Give the extent of all Plasmodium ovale-infected red blood cells.
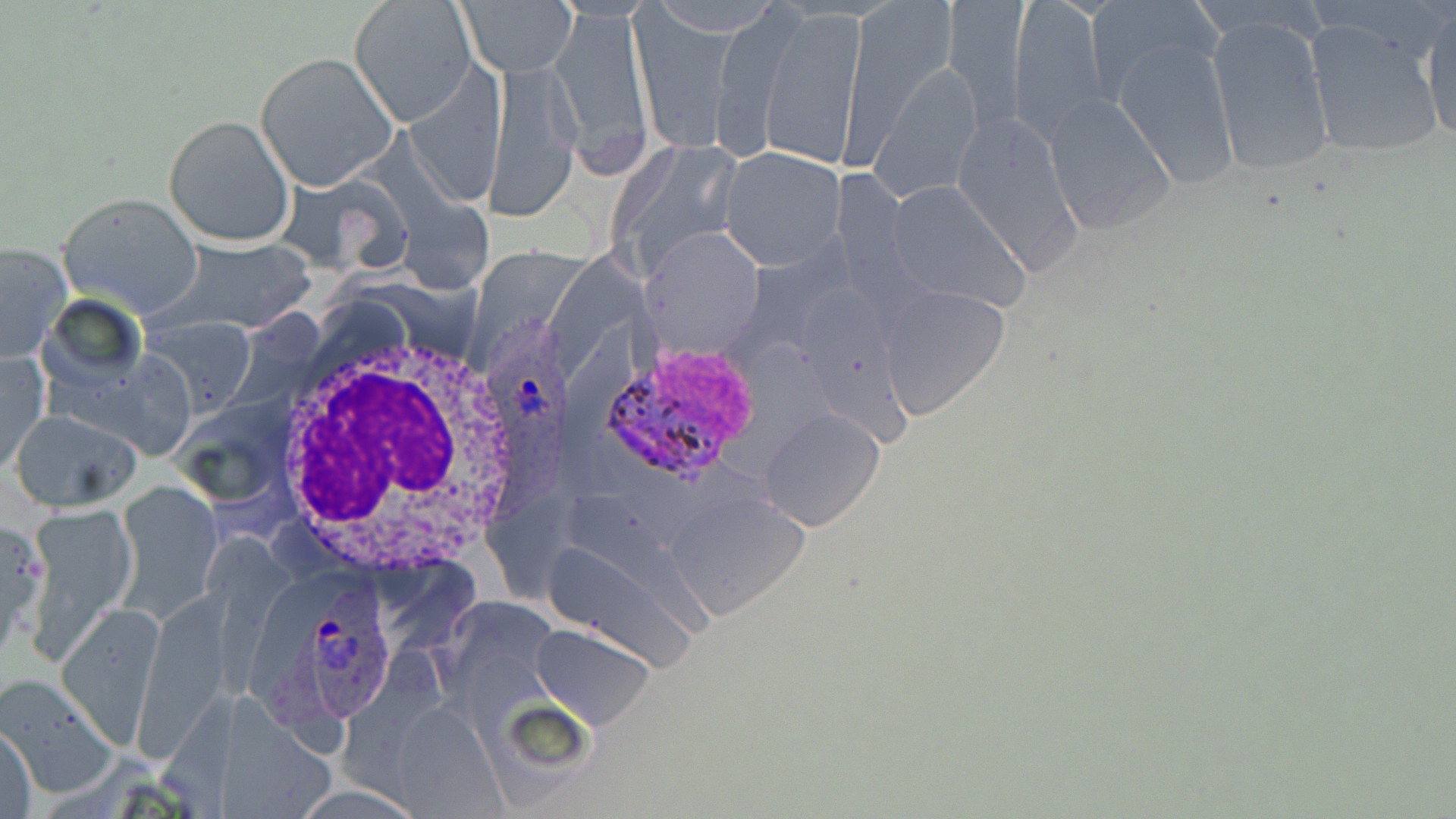
Approximate bounding boxes as (x1, y1, x2, y2) in pixels.
Plasmodium ovale-infected red blood cells: (484, 307, 573, 531), (592, 340, 761, 484), (253, 573, 399, 738).

Summary:
  - Uninfected red blood cell locations: (844, 0, 962, 152), (1008, 0, 1112, 141), (1086, 0, 1221, 103), (348, 1, 476, 127), (460, 1, 575, 78), (942, 3, 1029, 117), (550, 5, 652, 170), (759, 7, 867, 167), (1420, 8, 1455, 146), (630, 9, 732, 155), (1205, 14, 1336, 178), (1301, 17, 1445, 163), (1112, 38, 1239, 189), (256, 54, 397, 190), (487, 59, 583, 219), (1041, 93, 1176, 236), (947, 110, 1086, 272), (163, 114, 294, 247), (609, 134, 751, 276), (714, 147, 847, 270), (883, 180, 1029, 310), (57, 192, 203, 318), (166, 237, 317, 331), (0, 243, 71, 363), (879, 285, 1011, 420), (142, 319, 258, 416), (1, 352, 48, 474), (761, 408, 885, 531), (12, 410, 142, 510), (119, 482, 222, 616), (669, 493, 811, 620), (24, 505, 135, 658), (0, 518, 46, 662), (58, 599, 163, 744), (531, 623, 656, 730), (2, 673, 116, 796), (1, 724, 37, 817), (293, 781, 415, 817)
  - White blood cell locations: (264, 318, 532, 572)
  - Slide-level diagnosis: Plasmodium ovale
  - Modality: light microscopy
  - Preparation: thin blood smear
  - Magnification: 1000x
  - Field of view: one of a larger specimen
  - Image size: 1456×819 pixels
  - Stain: May-Grünwald-Giemsa